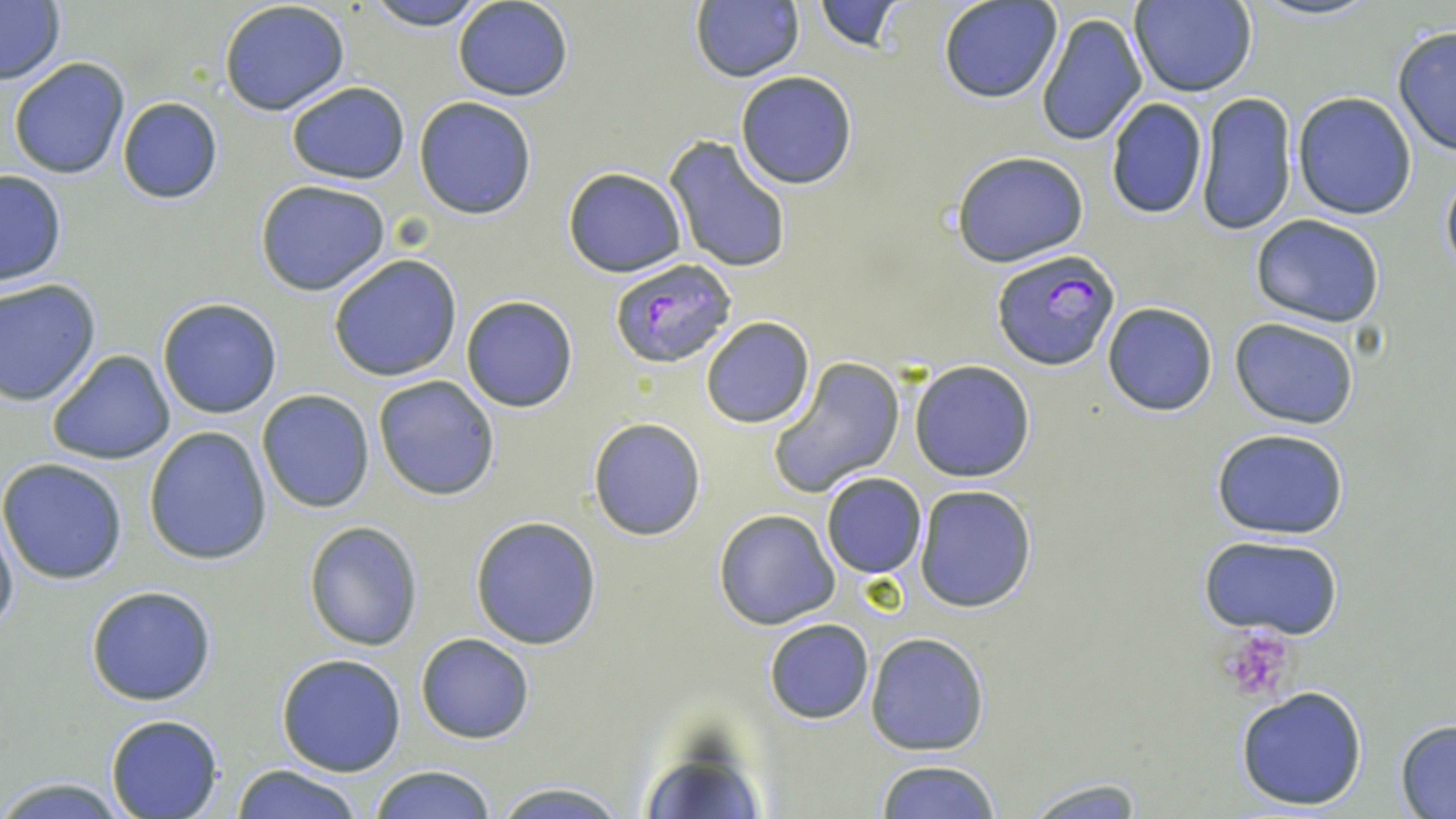
slide-level diagnosis = Plasmodium falciparum
modality = optical microscopy
stain = May-Grünwald-Giemsa
magnification = 1000x
Plasmodium falciparum-infected red blood cell locations = approximate bounding boxes as (x1,y1)-(x2,y2) corner pairs in pixels: (993,249)-(1120,371), (610,257)-(739,368)
preparation = thin blood smear
field of view = one of a larger specimen
platelet locations = approximate bounding boxes as (x1,y1)-(x2,y2) corner pairs in pixels: (1223,627)-(1299,702)
image size = 1456×819 pixels
uninfected red blood cell locations = approximate bounding boxes as (x1,y1)-(x2,y2) corner pairs in pixels: (364,0)-(490,27), (453,0)-(575,102), (814,0)-(905,53), (1250,0)-(1376,22), (0,1)-(66,85), (939,1)-(1061,103), (1128,1)-(1259,99), (218,2)-(351,117), (690,2)-(804,82), (1034,9)-(1148,149), (1391,24)-(1456,161), (8,57)-(132,179), (734,71)-(858,190), (286,80)-(410,185), (1293,92)-(1418,220), (1198,93)-(1297,236), (413,96)-(537,219), (116,97)-(222,204), (1104,98)-(1208,220), (663,136)-(793,275), (951,150)-(1089,267), (1440,163)-(1456,281), (563,167)-(688,278), (0,168)-(68,285), (255,180)-(391,296), (1251,214)-(1387,327), (329,254)-(462,380), (0,279)-(101,405), (460,296)-(579,412), (158,298)-(282,419), (1102,302)-(1218,416), (700,317)-(815,429), (1230,318)-(1359,428), (46,348)-(175,466), (768,356)-(906,499), (909,360)-(1037,483), (372,374)-(500,501), (257,389)-(374,513), (588,418)-(706,540), (1210,426)-(1349,539), (143,428)-(272,564), (0,458)-(127,584), (821,472)-(927,579), (913,485)-(1037,613), (713,508)-(840,630), (0,514)-(18,638), (470,515)-(602,650), (304,520)-(422,651), (1198,534)-(1347,638), (85,584)-(218,706), (763,618)-(874,724), (416,633)-(534,743), (865,633)-(991,755), (276,653)-(406,775), (1236,685)-(1369,812), (105,715)-(225,818), (1394,719)-(1456,816), (875,759)-(1004,818), (233,764)-(364,819), (370,766)-(496,819), (0,776)-(127,817), (1020,777)-(1148,816), (488,782)-(629,818)